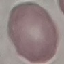
Result: negative for malaria parasites. Automatically extracted cell patch, resized to 64 × 64 pixels. Acquired by smartphone through the microscope eyepiece. Giemsa-stained preparation. Thin smear of blood.